Locate every malaria parasite.
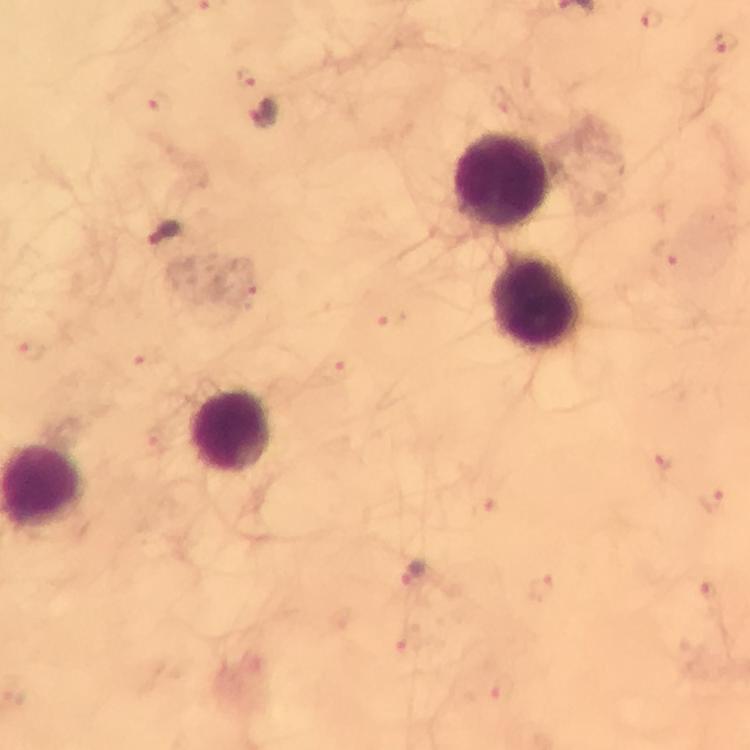

Approximate centers as [x, y] in pixels.
Malaria parasites: [726, 43], [264, 115], [165, 234], [414, 575].

Leukocyte locations: [505, 183], [540, 304], [230, 432]. Smartphone photograph taken through a microscope. Immersion oil was used. A crop from one field of view. Image is 750×750 pixels. Thick blood film. 100x magnification. From a diagnostic examination for malaria. Giemsa stain.